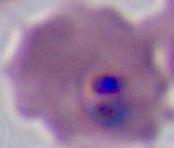
Summary:
  - Identification: Plasmodium
  - Magnification: 400x or 1000x
  - Modality: micrograph